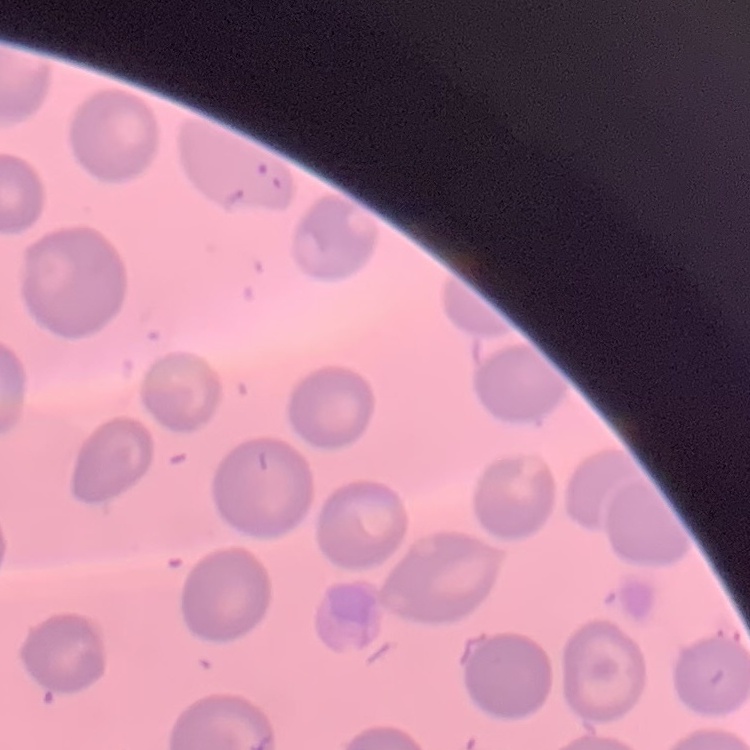

{
  "red_blood_cell_morphology": "no rouleaux formation",
  "stain": "Field's or Giemsa",
  "preparation": "thin blood film",
  "image_type": "square crop of a larger photomicrograph"
}